Locate every malaria parasite.
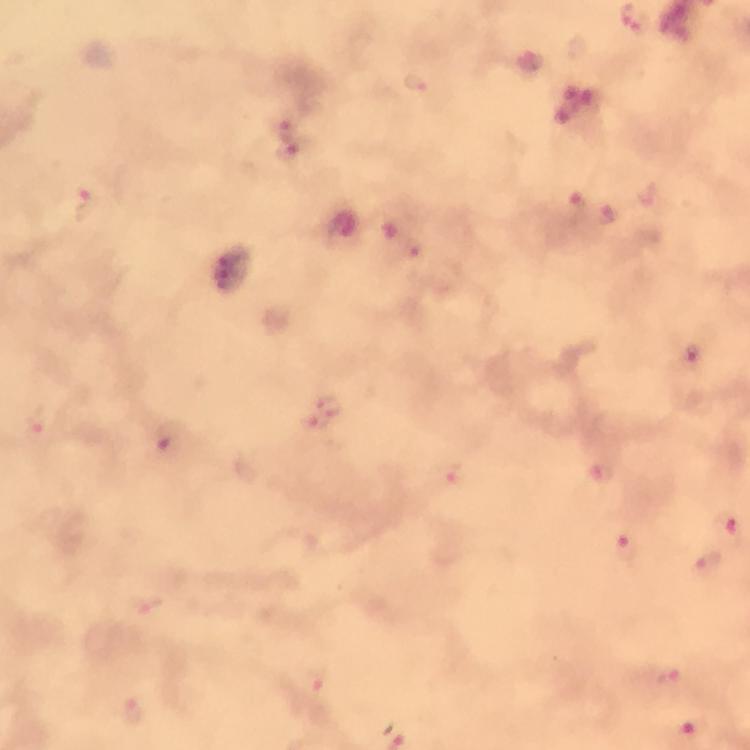

Approximate centers as [x, y] in pixels.
Malaria parasites: [416, 84], [289, 149], [87, 205], [606, 215], [412, 247], [694, 357], [325, 411], [162, 438], [447, 472], [600, 473], [729, 524], [628, 550], [706, 565], [667, 676], [316, 679], [135, 711].

image_size: 750×750 pixels
stain: Giemsa
context: from a malaria diagnostic workup
preparation: thick blood film
capture: smartphone photograph through a microscope
immersion_oil: applied
magnification: 100x
cropped_from: a single field of view